Evaluate for Plasmodium parasites.
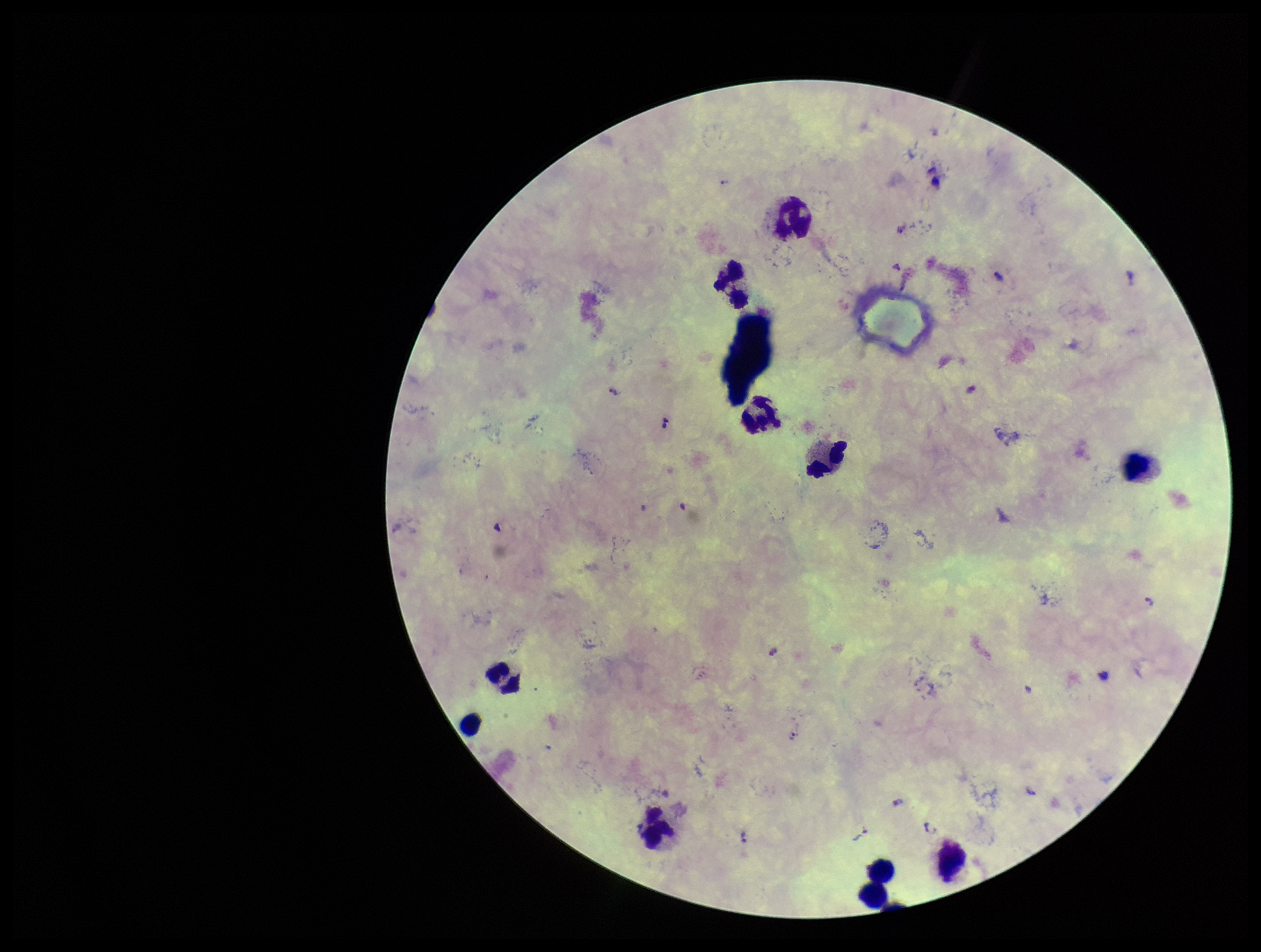
Detected.

{
  "stain": "Giemsa",
  "capture": "smartphone photograph through the microscope eyepiece",
  "preparation": "thick blood smear",
  "image_size": "1261×952 pixels",
  "species_reported_for_this_patient": "Plasmodium falciparum",
  "patient_malaria_status": "infected",
  "field_of_view": "one from this slide",
  "leukocyte_count": 10,
  "parasite_count": 10
}